State which parasite is depicted.
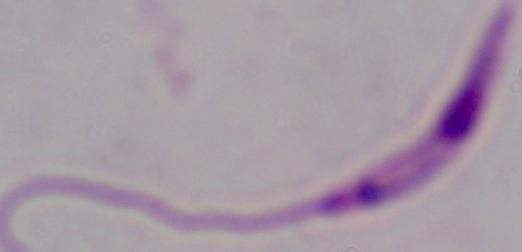

Leishmania.

{
  "magnification": "1000x",
  "modality": "micrograph"
}